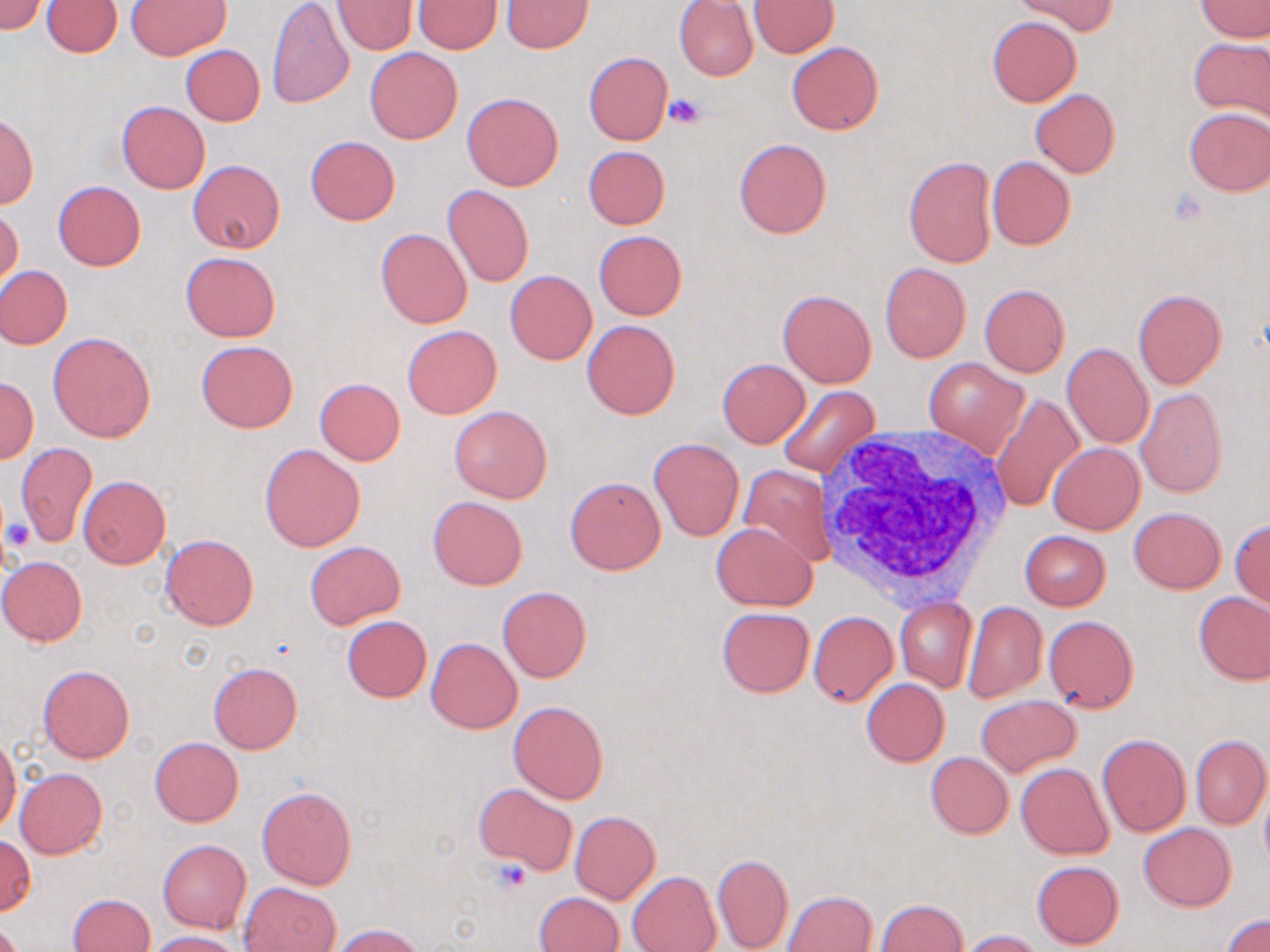

slide-level diagnosis = negative for blood parasites
white blood cell locations = approximate bounding boxes as [x1, y1, x2, y2] in pixels: [819, 427, 1017, 607]
uninfected red blood cell locations = approximate bounding boxes as [x1, y1, x2, y2] in pixels: [0, 0, 43, 36], [43, 0, 123, 58], [266, 0, 354, 109], [333, 0, 418, 54], [413, 0, 501, 53], [747, 0, 839, 57], [1196, 0, 1270, 41], [127, 1, 231, 60], [502, 1, 592, 52], [674, 1, 759, 81], [1017, 1, 1116, 36], [987, 16, 1081, 106], [1189, 36, 1270, 128], [786, 41, 883, 135], [180, 44, 265, 127], [365, 48, 462, 143], [583, 52, 673, 146], [1029, 88, 1120, 177], [462, 92, 563, 191], [117, 101, 209, 192], [1182, 106, 1270, 195], [0, 115, 38, 207], [306, 136, 400, 224], [734, 139, 831, 238], [582, 145, 669, 229], [902, 156, 996, 268], [987, 156, 1075, 249], [188, 160, 285, 253], [53, 181, 145, 271], [442, 184, 534, 287], [1, 204, 22, 291], [376, 228, 472, 328], [594, 230, 686, 319], [180, 252, 280, 341], [880, 262, 970, 361], [0, 267, 72, 349], [504, 270, 597, 364], [979, 284, 1069, 376], [779, 289, 876, 387], [1132, 289, 1226, 388], [582, 319, 679, 419], [402, 325, 501, 418], [47, 331, 157, 442], [196, 339, 299, 433], [1062, 343, 1154, 449], [717, 358, 810, 447], [924, 359, 1028, 457], [1, 378, 37, 463], [316, 378, 405, 464], [776, 386, 878, 479], [1135, 387, 1227, 498], [990, 392, 1083, 512], [449, 405, 552, 504], [649, 437, 744, 540], [1049, 442, 1144, 534], [13, 443, 97, 547], [259, 443, 366, 551], [740, 465, 831, 567], [78, 475, 170, 568], [565, 476, 665, 575], [428, 495, 527, 590], [1129, 507, 1226, 593], [1230, 519, 1270, 610], [711, 521, 817, 610], [1020, 531, 1110, 609], [161, 534, 258, 630], [304, 541, 404, 629], [0, 556, 87, 645], [498, 586, 591, 682], [1195, 592, 1270, 684], [894, 597, 976, 692], [962, 601, 1047, 703], [717, 608, 814, 697], [809, 611, 897, 706], [341, 616, 431, 702], [1044, 616, 1139, 711], [426, 637, 521, 733], [208, 662, 302, 754], [38, 664, 133, 763], [862, 678, 950, 766], [976, 694, 1079, 776], [508, 701, 609, 802], [1097, 734, 1191, 837], [1190, 735, 1270, 830], [0, 736, 20, 833], [149, 737, 242, 826], [925, 752, 1012, 837], [1016, 762, 1113, 859], [15, 767, 107, 858], [475, 782, 577, 874], [1259, 784, 1270, 870], [257, 785, 355, 889], [570, 811, 660, 903], [1139, 822, 1235, 912], [1, 833, 35, 916], [157, 839, 250, 932], [711, 852, 793, 952], [1031, 860, 1123, 948], [627, 871, 721, 952], [239, 883, 339, 952], [783, 890, 877, 951], [69, 892, 154, 952], [534, 892, 622, 952], [874, 899, 968, 952], [1222, 913, 1270, 952], [330, 924, 427, 952], [960, 929, 1045, 951], [148, 930, 245, 952]
stain = May-Grünwald-Giemsa
preparation = thin blood film
field of view = one of a larger specimen
image size = 1270×952 pixels
magnification = 1000x
platelet locations = approximate bounding boxes as [x1, y1, x2, y2] in pixels: [666, 93, 708, 129], [1167, 189, 1207, 227], [4, 519, 34, 549], [490, 857, 530, 893]
modality = optical microscopy